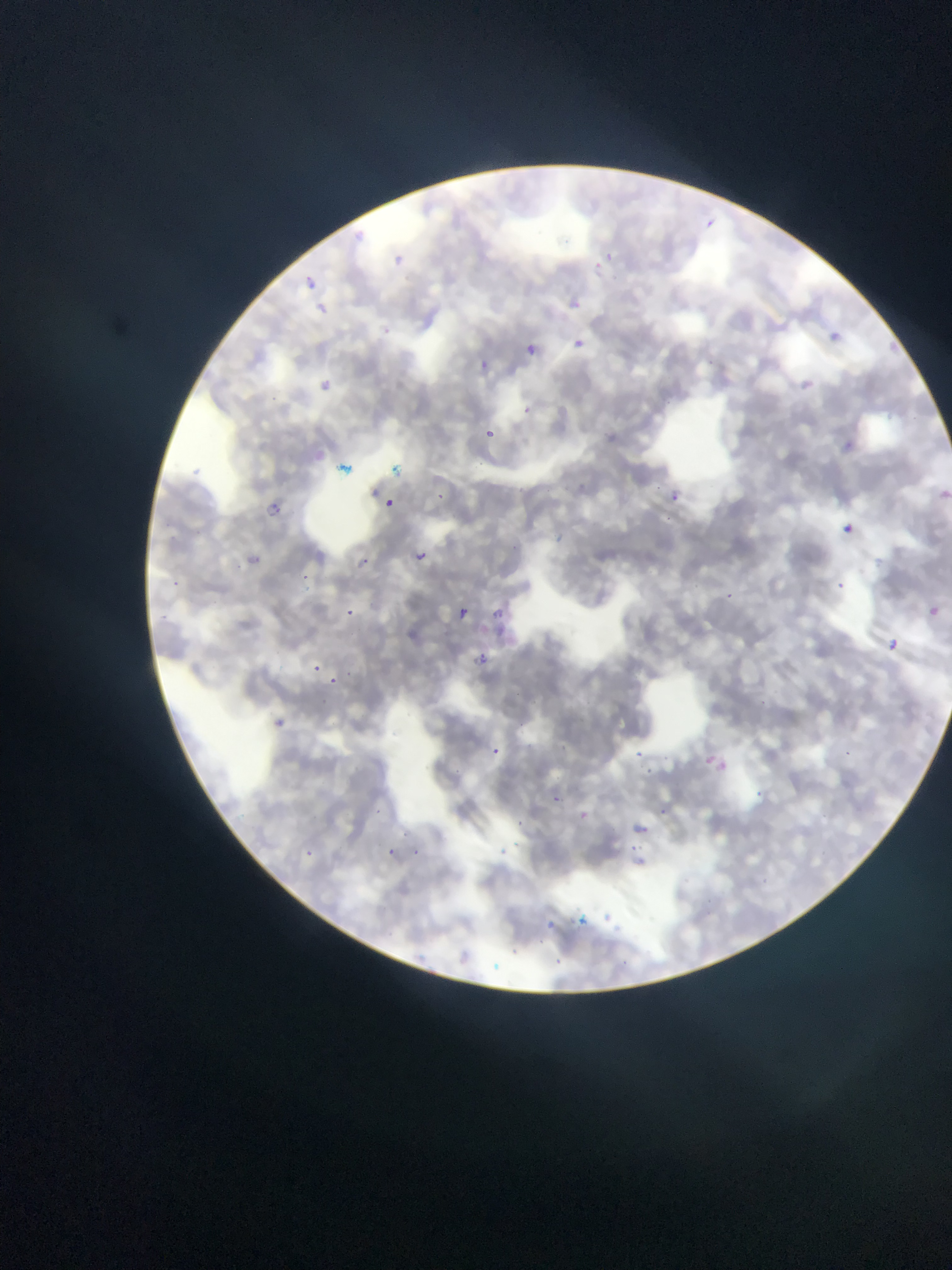
preparation = thin blood smear
capture = mobile-phone photograph through a microscope
field of view = single
malaria parasite locations = approximate bounding boxes as {left, top, right, bottom} in pixels: {702, 216, 719, 229}, {355, 232, 369, 245}, {603, 247, 617, 262}, {391, 251, 419, 275}, {594, 258, 603, 274}, {305, 275, 318, 289}, {572, 297, 585, 310}, {314, 301, 331, 316}, {381, 323, 402, 341}, {828, 329, 848, 346}, {889, 335, 905, 352}, {570, 336, 589, 348}, {524, 343, 537, 355}, {479, 358, 492, 372}, {310, 372, 333, 396}, {797, 373, 819, 388}, {522, 404, 533, 414}, {886, 409, 909, 418}, {486, 426, 501, 441}, {839, 431, 854, 452}, {195, 466, 204, 479}, {938, 489, 950, 501}, {669, 490, 683, 502}, {385, 497, 395, 507}, {269, 502, 279, 514}, {843, 522, 855, 533}, {417, 547, 430, 561}, {359, 552, 379, 566}, {249, 557, 256, 566}, {300, 569, 312, 586}, {173, 577, 191, 590}, {835, 580, 845, 589}, {723, 589, 737, 602}, {460, 604, 476, 620}, {927, 604, 939, 617}, {343, 609, 361, 620}, {494, 609, 510, 628}, {888, 638, 899, 650}, {472, 651, 486, 665}, {311, 658, 324, 673}, {326, 673, 339, 686}, {269, 713, 289, 726}, {491, 744, 503, 757}, {634, 746, 646, 761}, {842, 746, 855, 757}, {705, 754, 729, 770}, {641, 760, 658, 780}, {755, 784, 765, 797}, {547, 792, 561, 803}, {659, 799, 674, 819}, {372, 806, 383, 815}, {573, 807, 589, 822}, {628, 820, 648, 832}, {401, 825, 410, 838}, {631, 841, 646, 854}, {300, 845, 317, 858}, {409, 846, 422, 855}, {383, 847, 398, 861}, {494, 847, 518, 860}, {541, 916, 554, 938}, {509, 947, 523, 956}
image size = 952×1270 pixels
country = Ghana